Describe the morphology of the erythrocytes.
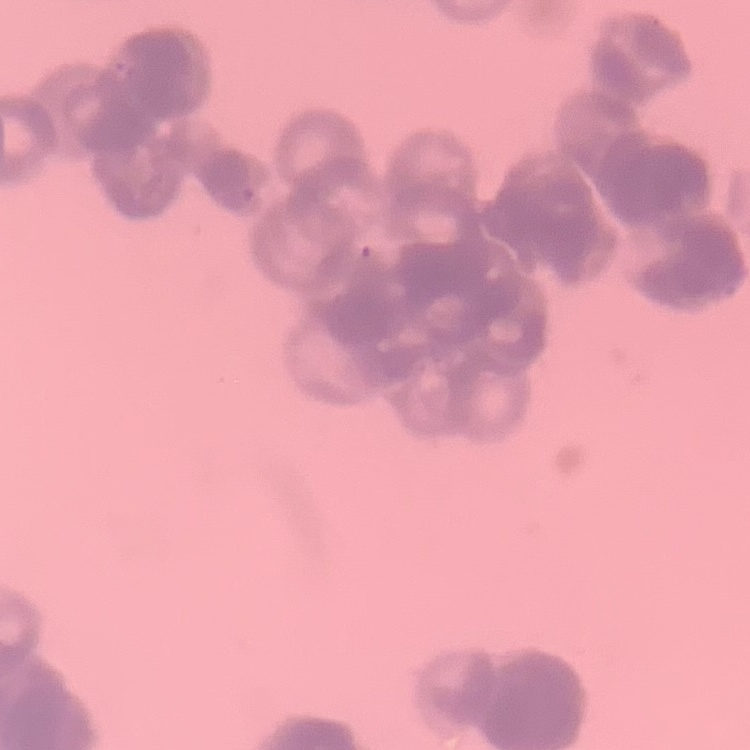

Rouleaux formation.

Stained with either Field's or Giemsa. Thin blood film. One tile cut from a larger photomicrograph.